Name the parasite shown.
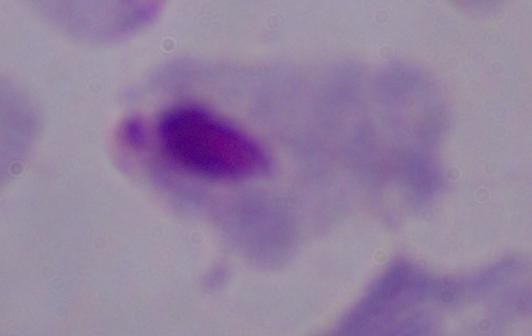

This is a trichomonad.

{
  "modality": "photomicrograph",
  "magnification": "1000x"
}